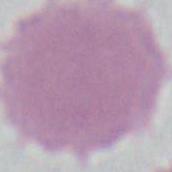
Summary:
  - Modality: photomicrograph
  - Magnification: 1000x
  - Identification: erythrocyte